Report the malaria status of this cell.
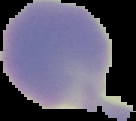

Uninfected.

image type = segmented cell region on a black background
preparation = thin blood smear
image size = 136×121 pixels